Locate and identify every blood parasite.
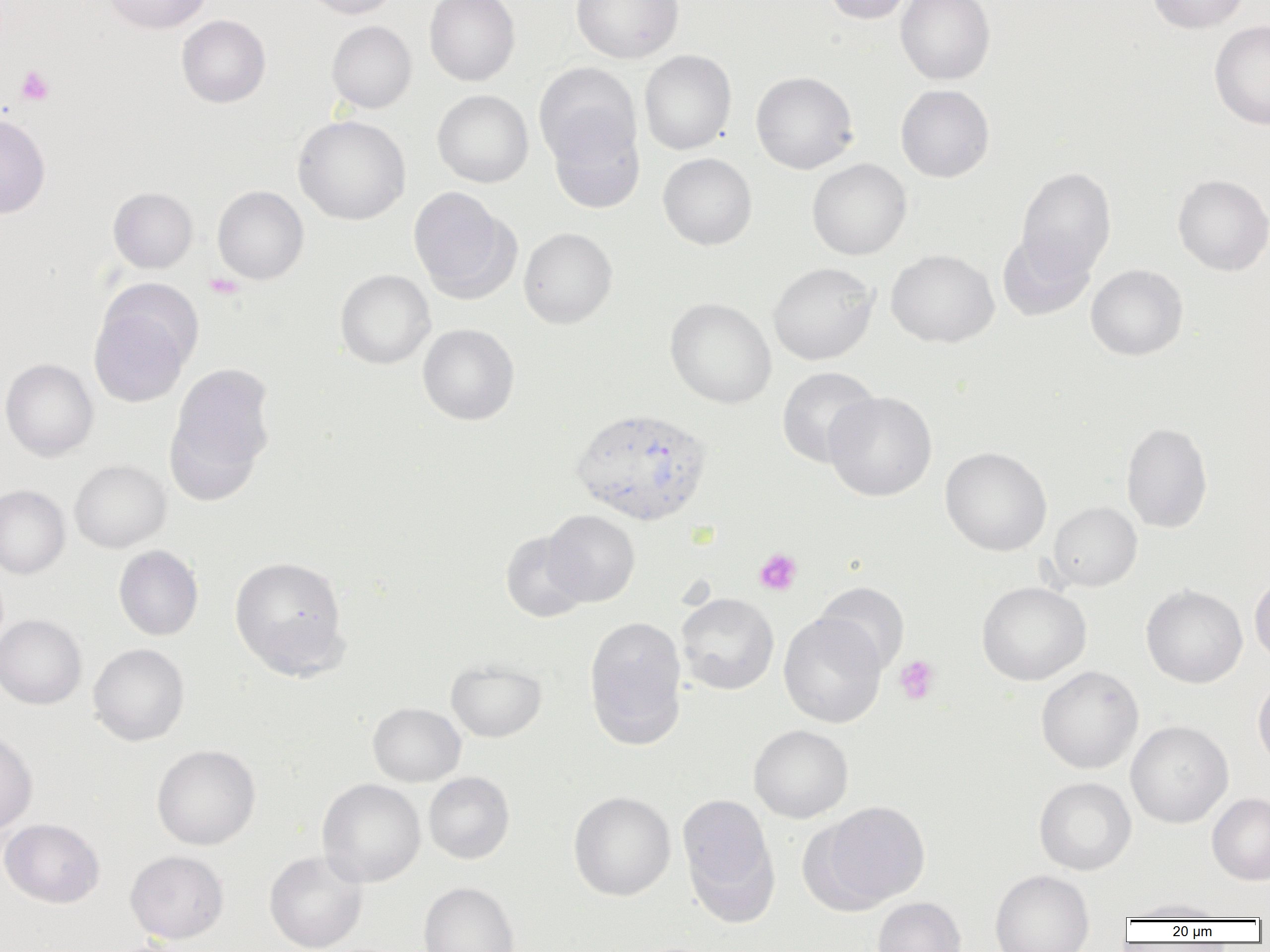

Approximate bounding boxes as named x1/y1/x2/y2 corners in pixels.
Plasmodium vivax-infected red blood cells: (x1=570, y1=407, x2=713, y2=527).
No Plasmodium falciparum, Plasmodium ovale, Plasmodium malariae, Babesia divergens, or Trypanosoma brucei observed.

Summary:
  - Platelet locations: (x1=16, y1=65, x2=54, y2=106), (x1=204, y1=273, x2=245, y2=300), (x1=753, y1=548, x2=803, y2=596), (x1=893, y1=655, x2=940, y2=705)
  - Uninfected red blood cell locations: (x1=103, y1=0, x2=211, y2=34), (x1=301, y1=0, x2=401, y2=19), (x1=424, y1=0, x2=520, y2=86), (x1=571, y1=0, x2=684, y2=63), (x1=821, y1=0, x2=916, y2=24), (x1=896, y1=0, x2=996, y2=85), (x1=1147, y1=0, x2=1251, y2=33), (x1=177, y1=14, x2=271, y2=107), (x1=326, y1=20, x2=417, y2=113), (x1=1210, y1=20, x2=1270, y2=130), (x1=639, y1=50, x2=737, y2=155), (x1=534, y1=63, x2=641, y2=168), (x1=751, y1=71, x2=859, y2=174), (x1=895, y1=84, x2=995, y2=183), (x1=432, y1=89, x2=533, y2=188), (x1=0, y1=114, x2=50, y2=219), (x1=293, y1=115, x2=411, y2=225), (x1=548, y1=115, x2=645, y2=213), (x1=658, y1=153, x2=757, y2=251), (x1=807, y1=158, x2=912, y2=260), (x1=1016, y1=167, x2=1117, y2=280), (x1=1172, y1=174, x2=1270, y2=276), (x1=212, y1=185, x2=309, y2=285), (x1=408, y1=186, x2=517, y2=301), (x1=108, y1=187, x2=198, y2=273), (x1=519, y1=227, x2=617, y2=328), (x1=997, y1=231, x2=1095, y2=322), (x1=886, y1=249, x2=999, y2=348), (x1=768, y1=262, x2=879, y2=365), (x1=1086, y1=264, x2=1188, y2=361), (x1=335, y1=269, x2=435, y2=369), (x1=665, y1=298, x2=777, y2=408), (x1=89, y1=300, x2=193, y2=408), (x1=417, y1=323, x2=519, y2=425), (x1=0, y1=358, x2=99, y2=461), (x1=166, y1=362, x2=276, y2=495), (x1=776, y1=366, x2=881, y2=468), (x1=824, y1=391, x2=937, y2=501), (x1=1120, y1=422, x2=1214, y2=533), (x1=940, y1=447, x2=1052, y2=556), (x1=70, y1=460, x2=171, y2=553), (x1=0, y1=484, x2=71, y2=579), (x1=1047, y1=502, x2=1142, y2=591), (x1=543, y1=510, x2=640, y2=606), (x1=500, y1=530, x2=590, y2=623), (x1=113, y1=545, x2=203, y2=641), (x1=229, y1=555, x2=349, y2=677), (x1=1249, y1=574, x2=1270, y2=666), (x1=814, y1=581, x2=910, y2=676), (x1=977, y1=581, x2=1092, y2=686), (x1=1141, y1=585, x2=1248, y2=687), (x1=676, y1=593, x2=779, y2=695), (x1=778, y1=613, x2=887, y2=728), (x1=0, y1=615, x2=87, y2=709), (x1=584, y1=616, x2=687, y2=748), (x1=88, y1=643, x2=190, y2=746), (x1=446, y1=659, x2=546, y2=742), (x1=1036, y1=665, x2=1144, y2=774), (x1=1252, y1=675, x2=1270, y2=769), (x1=367, y1=702, x2=466, y2=787), (x1=1125, y1=720, x2=1233, y2=828), (x1=749, y1=724, x2=853, y2=823), (x1=0, y1=729, x2=37, y2=834), (x1=152, y1=744, x2=261, y2=850), (x1=423, y1=772, x2=515, y2=864), (x1=1033, y1=776, x2=1136, y2=875), (x1=317, y1=778, x2=426, y2=887), (x1=568, y1=791, x2=676, y2=901), (x1=677, y1=792, x2=779, y2=916), (x1=1207, y1=793, x2=1270, y2=885), (x1=817, y1=800, x2=930, y2=909), (x1=0, y1=818, x2=104, y2=908), (x1=125, y1=850, x2=229, y2=943), (x1=264, y1=851, x2=367, y2=952), (x1=990, y1=869, x2=1094, y2=952), (x1=418, y1=882, x2=519, y2=952), (x1=872, y1=897, x2=966, y2=952), (x1=1123, y1=898, x2=1231, y2=920), (x1=103, y1=937, x2=196, y2=952)
  - Slide-level diagnosis: Plasmodium vivax
  - Field of view: one of a larger specimen
  - Magnification: 1000x
  - Image size: 1270×952 pixels
  - Preparation: thin blood film
  - Modality: optical microscopy